Identify the parasite.
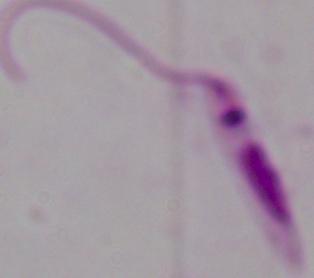

Leishmania.

Summary:
  - Modality: photomicrograph
  - Magnification: 1000x